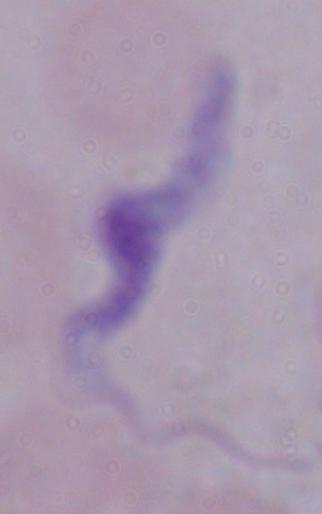

Summary:
  - Magnification: 1000x
  - Identification: trypanosome
  - Modality: micrograph